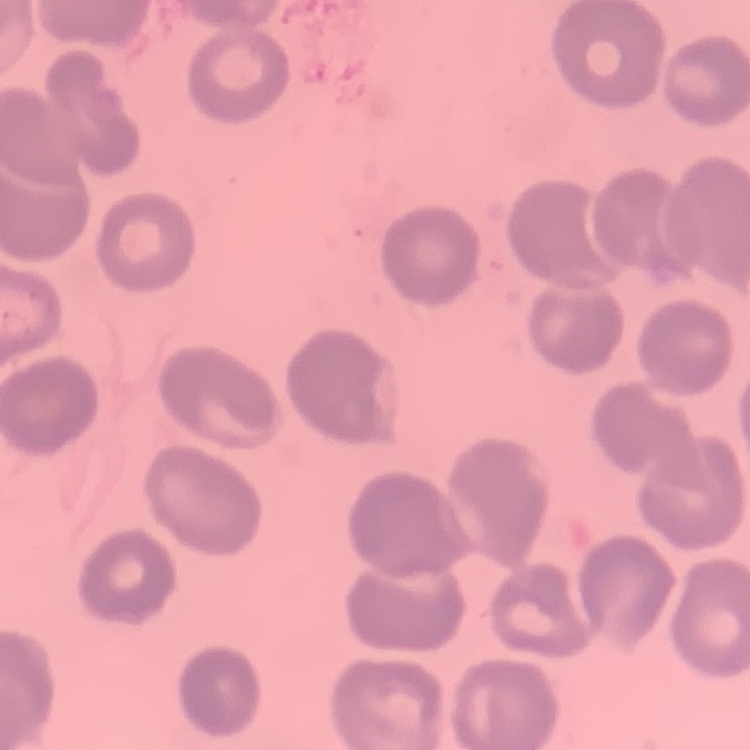

Summary:
  - Erythrocyte morphology: no rouleaux formation
  - Image type: square crop of a larger photomicrograph
  - Stain: Field's or Giemsa
  - Preparation: thin peripheral smear